Comment on the morphology of the red blood cells.
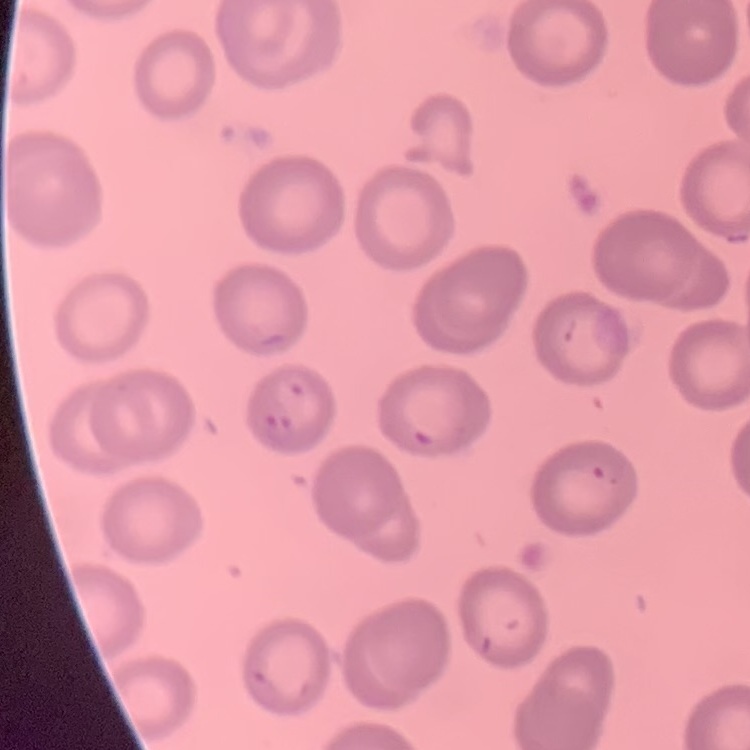
They show no rouleaux formation.

stain = Field's or Giemsa
image type = square crop of a larger photomicrograph
preparation = thin blood film